Identify the preparation type.
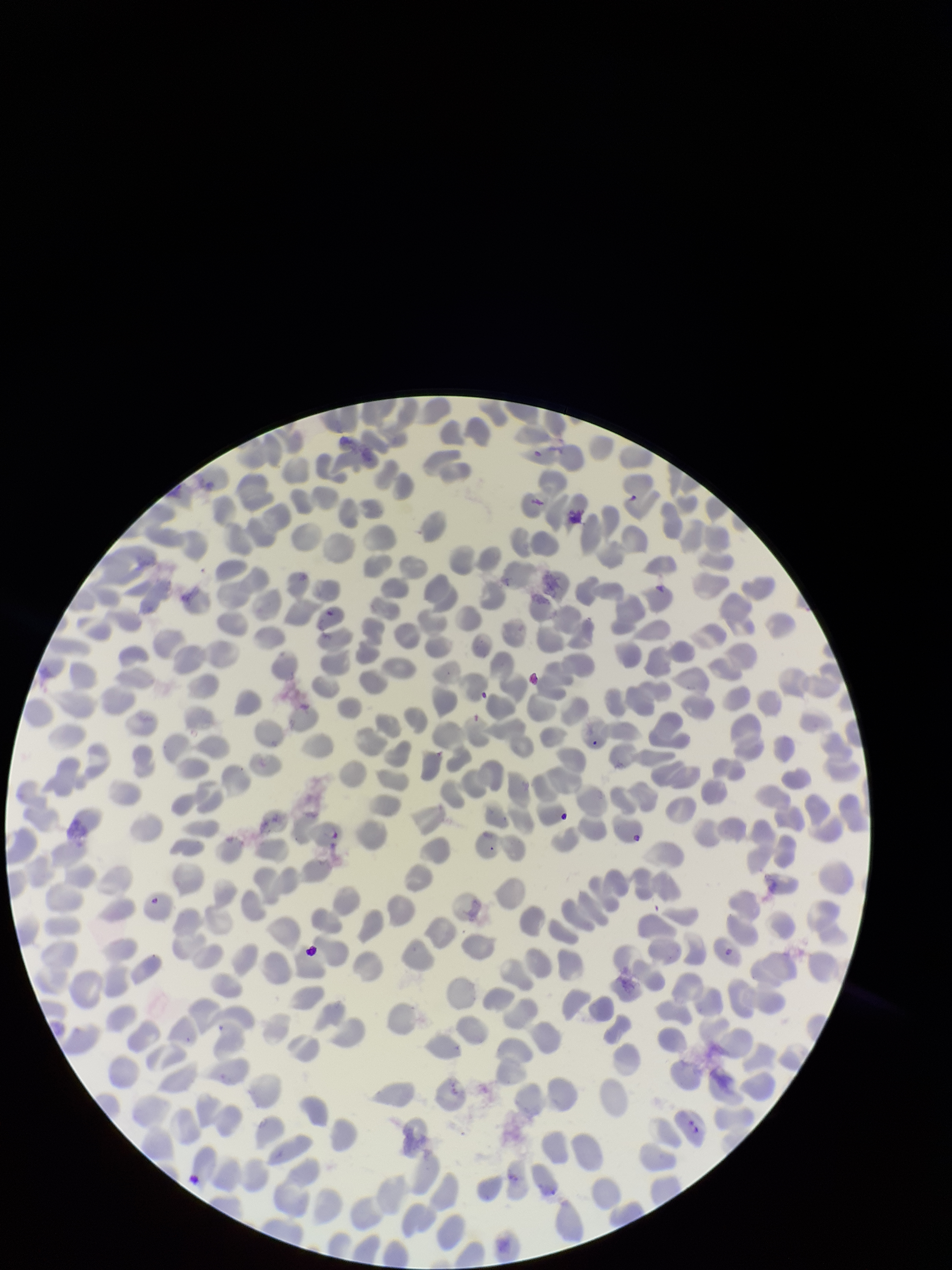
It is a thin blood smear.

Summary:
  - Stain: Giemsa
  - Image size: 952×1270 pixels
  - Field of view: single
  - Parasitized red blood cell count: 2
  - Patient malaria status: infected
  - Red blood cell count: 362
  - Capture: smartphone photograph through the microscope eyepiece
  - Species reported for this patient: Plasmodium falciparum
  - Parasitized red blood cells: identified